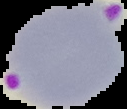

preparation = thin blood film
image type = segmented cell region with the area outside set to black
malaria status = parasitized
image size = 127×109 pixels